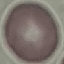

Malaria status: uninfected. Thin smear of blood. Acquired by smartphone through the microscope eyepiece. Giemsa stain. Automatically extracted cell patch, resized to 64 × 64 pixels.